Assess this cell for malaria.
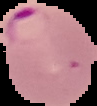
Parasitized.

Summary:
  - Image type: cell region segmented out of the field of view; surrounding area masked to black
  - Preparation: thin blood film
  - Image size: 97×106 pixels